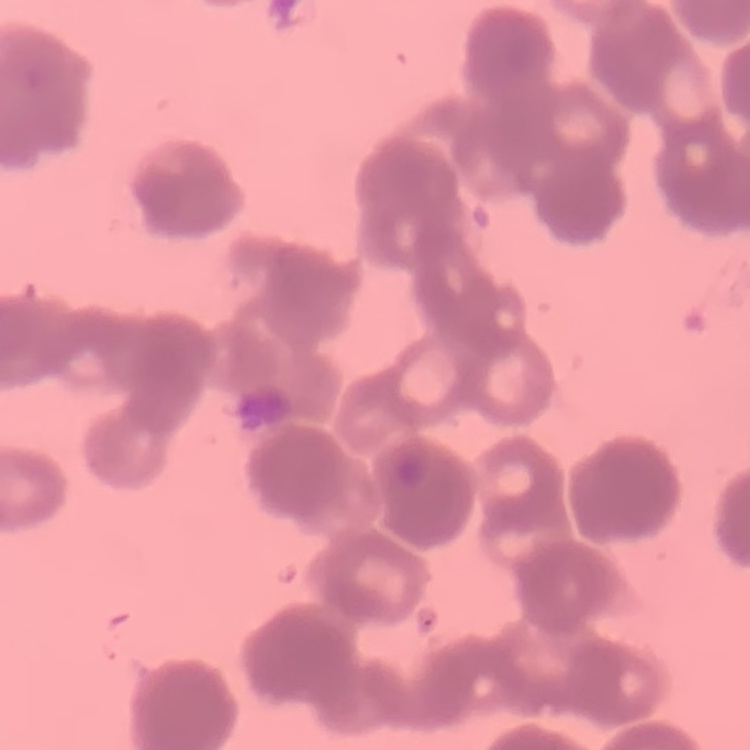
red blood cell morphology = rouleaux formation
preparation = thin peripheral smear
stain = Field's or Giemsa
image type = square crop of a larger photomicrograph